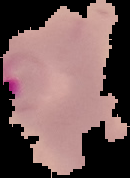
image_size: 130×178 pixels
preparation: thin blood smear
result: Plasmodium parasites detected
image_type: cell region segmented out of the field of view; surrounding area masked to black